Locate every blood parasite and identify its species.
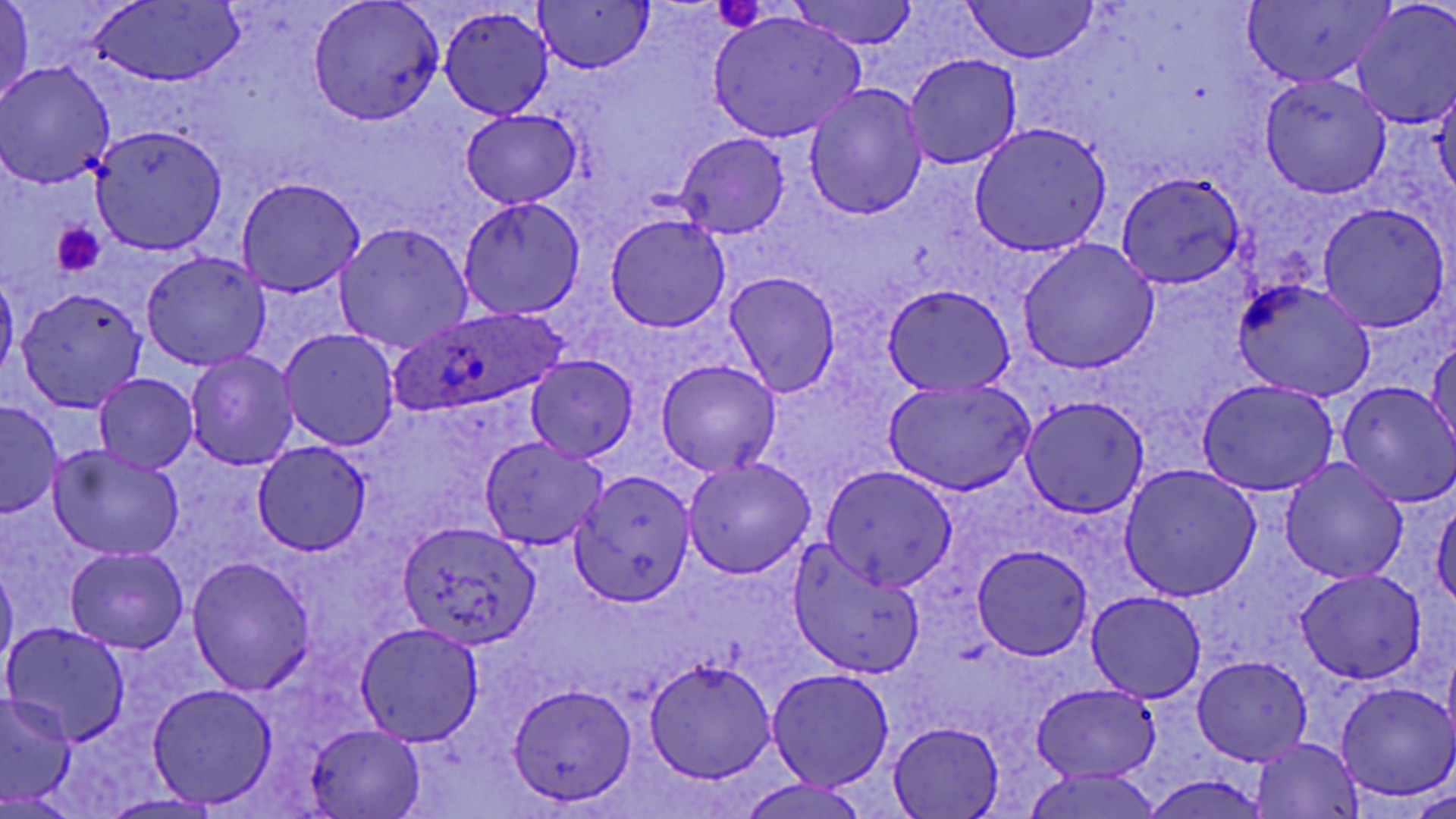

Approximate bounding boxes as (x1, y1, x2, y2) in pixels.
Plasmodium ovale-infected red blood cells: (389, 306, 570, 418).
No Plasmodium falciparum, Plasmodium malariae, Plasmodium vivax, Babesia divergens, or Trypanosoma brucei observed.

Uninfected red blood cell locations: (0, 0, 35, 108), (307, 0, 442, 125), (782, 0, 923, 50), (959, 0, 1101, 67), (1241, 1, 1394, 87), (89, 3, 241, 83), (535, 3, 653, 74), (1351, 5, 1456, 127), (439, 6, 553, 120), (706, 11, 867, 142), (1292, 33, 1451, 175), (904, 54, 1021, 171), (0, 62, 116, 189), (1260, 74, 1393, 198), (1433, 77, 1456, 202), (804, 82, 928, 221), (461, 111, 580, 209), (969, 122, 1111, 256), (89, 126, 227, 254), (675, 132, 790, 239), (1116, 173, 1245, 287), (235, 177, 366, 297), (458, 196, 586, 319), (1317, 203, 1451, 332), (604, 214, 731, 333), (336, 223, 473, 352), (1018, 240, 1157, 373), (141, 251, 273, 370), (0, 272, 19, 381), (724, 272, 841, 398), (1231, 280, 1375, 404), (883, 284, 1016, 397), (17, 287, 148, 411), (279, 328, 401, 451), (1428, 336, 1455, 452), (186, 349, 299, 469), (527, 355, 637, 460), (656, 359, 781, 477), (95, 373, 198, 472), (883, 379, 1034, 496), (1197, 379, 1338, 495), (1335, 381, 1456, 508), (1019, 394, 1150, 518), (0, 401, 64, 518), (479, 438, 606, 549), (253, 441, 372, 555), (47, 446, 186, 563), (682, 457, 815, 578), (1280, 457, 1408, 585), (1119, 463, 1261, 601), (821, 464, 959, 593), (567, 470, 696, 605), (1294, 475, 1422, 665), (1432, 500, 1456, 611), (397, 520, 539, 647), (788, 544, 928, 678), (972, 545, 1092, 659), (66, 546, 187, 652), (187, 557, 315, 695), (1, 559, 17, 670), (1294, 569, 1427, 685), (1086, 591, 1208, 704), (3, 623, 131, 745), (355, 623, 484, 746), (1193, 655, 1311, 766), (643, 659, 777, 783), (767, 668, 895, 790), (1030, 682, 1162, 782), (1336, 682, 1456, 801), (509, 683, 635, 806), (146, 685, 277, 808), (0, 693, 76, 806), (886, 722, 1003, 818), (304, 723, 424, 818), (1252, 738, 1364, 817), (1022, 768, 1166, 819), (1143, 771, 1273, 818), (737, 779, 872, 819), (1415, 789, 1455, 818), (0, 791, 79, 817), (98, 794, 222, 818). Platelet locations: (714, 2, 769, 32), (53, 223, 104, 274). Slide-level diagnosis: Plasmodium ovale. Image is 1456×819 pixels. Thin blood film. Light microscopy. May-Grünwald-Giemsa stain. One field of a larger specimen. 1000x magnification.